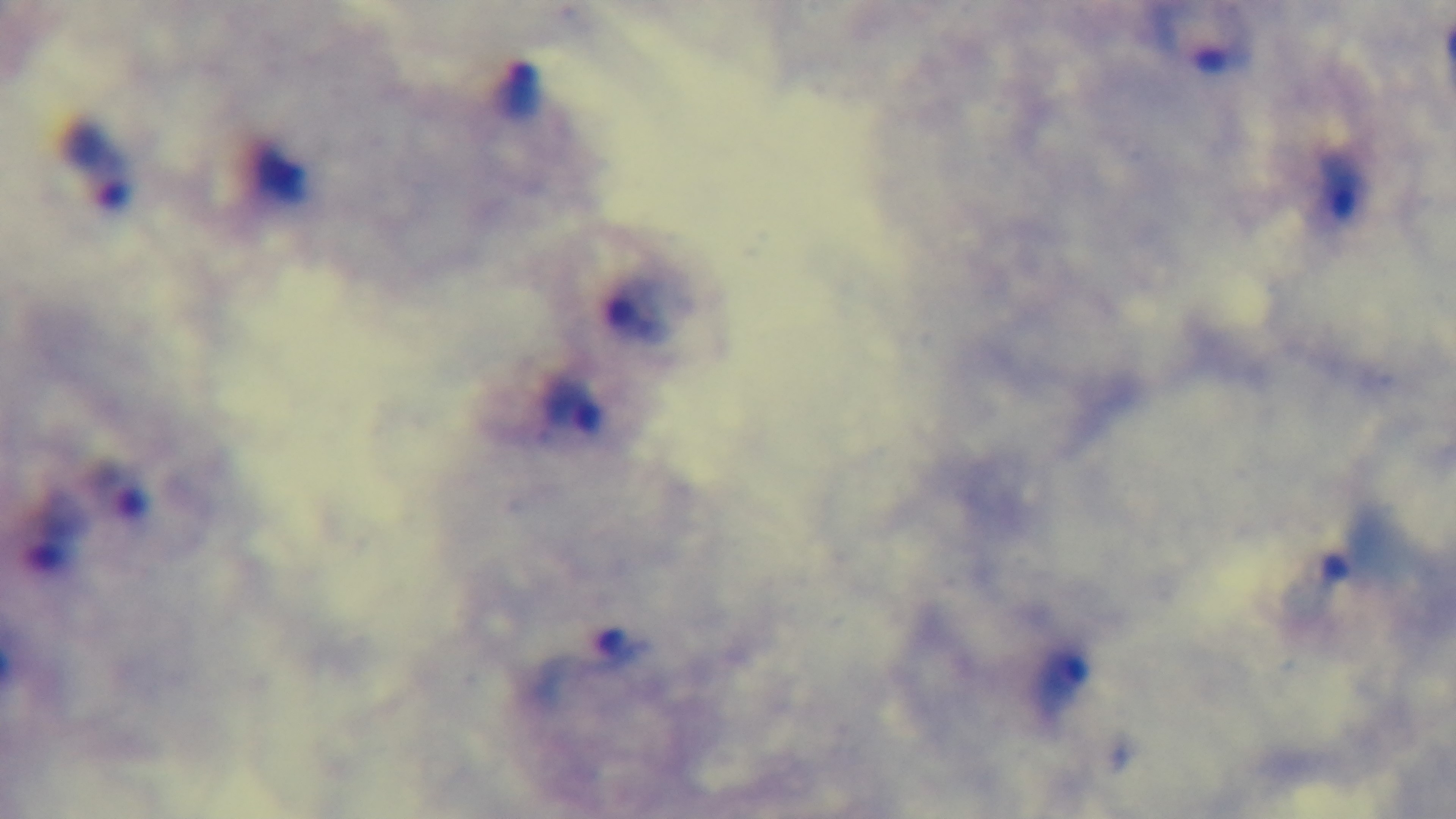

stain: Giemsa
capture: mounted 4K digital camera
preparation: thick blood film
malaria_status: positive
field_of_view: single
objective: 100x oil immersion
modality: light microscopy